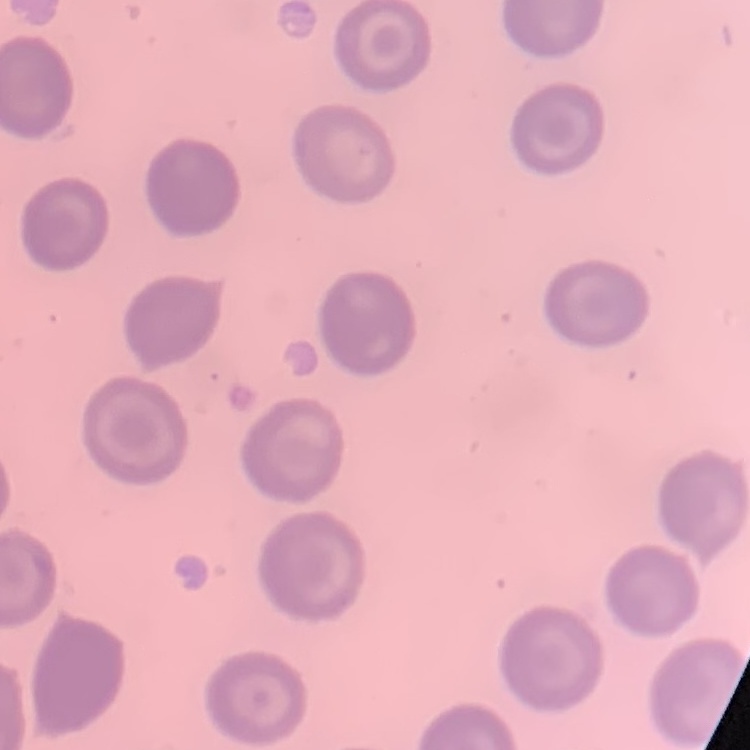

The erythrocytes show no rouleaux formation. Stained with either Field's or Giemsa. One tile cut from a larger photomicrograph. Thin blood smear.